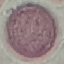 Result: no malaria parasites detected. Giemsa stain. Cell patch, automatically extracted from a larger field of view and resized to 64 × 64 pixels. Photographed with a smartphone camera at the microscope eyepiece. Thin blood film.